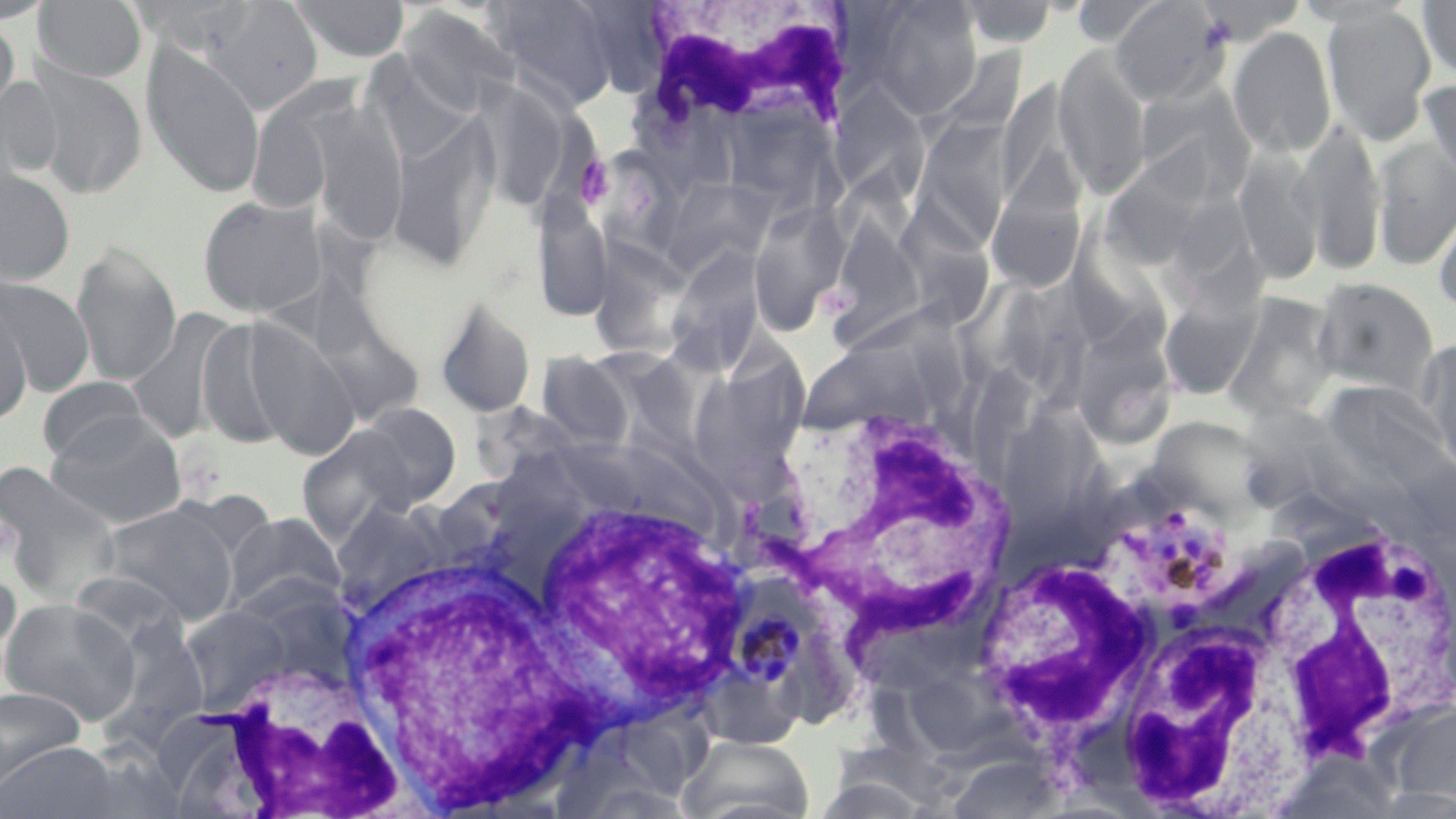

slide-level diagnosis = Plasmodium malariae
image size = 1456×819 pixels
white blood cell locations = approximate bounding boxes as [x1, y1, x2, y2] in pixels: [639, 0, 854, 131], [778, 403, 1019, 653], [516, 487, 753, 722], [1246, 504, 1451, 766], [331, 543, 604, 816], [970, 552, 1154, 744], [1108, 607, 1305, 814], [189, 661, 409, 818]
Plasmodium malariae-infected red blood cell locations = approximate bounding boxes as [x1, y1, x2, y2] in pixels: [1097, 492, 1240, 610], [727, 573, 819, 695]
preparation = thin blood film
magnification = 1000x
platelet locations = approximate bounding boxes as [x1, y1, x2, y2] in pixels: [575, 156, 615, 208]
field of view = one of a larger specimen
uninfected red blood cell locations = approximate bounding boxes as [x1, y1, x2, y2] in pixels: [33, 0, 147, 83], [128, 0, 260, 58], [206, 0, 324, 113], [289, 0, 410, 64], [484, 0, 622, 112], [861, 0, 984, 120], [1068, 0, 1169, 47], [1194, 0, 1307, 44], [1419, 0, 1456, 80], [956, 1, 1059, 48], [1110, 1, 1227, 105], [1323, 4, 1437, 146], [405, 6, 525, 116], [0, 14, 20, 122], [1229, 26, 1337, 158], [357, 34, 467, 156], [140, 41, 267, 199], [938, 47, 1026, 137], [1054, 47, 1152, 199], [26, 65, 149, 199], [0, 77, 63, 187], [1421, 78, 1456, 188], [997, 80, 1088, 211], [468, 83, 575, 210], [1134, 84, 1256, 200], [829, 87, 930, 203], [296, 98, 411, 248], [388, 114, 500, 273], [911, 117, 1017, 247], [1298, 118, 1386, 276], [1373, 137, 1456, 270], [987, 140, 1089, 290], [1098, 140, 1220, 270], [594, 147, 686, 273], [1235, 148, 1324, 285], [0, 166, 77, 286], [664, 180, 784, 285], [198, 194, 328, 319], [533, 194, 613, 323], [1433, 197, 1456, 319], [749, 199, 852, 335], [902, 203, 995, 333], [823, 207, 930, 345], [1077, 215, 1172, 347], [70, 240, 183, 388], [665, 249, 764, 378], [589, 266, 685, 367], [0, 277, 95, 397], [1311, 278, 1439, 399], [1158, 285, 1265, 401], [310, 289, 424, 434], [1223, 292, 1340, 423], [0, 294, 33, 426], [434, 295, 536, 418], [130, 308, 238, 444], [237, 314, 361, 460], [1085, 316, 1180, 447], [195, 317, 299, 449], [802, 330, 936, 436], [739, 332, 811, 462], [1420, 337, 1456, 475], [537, 352, 635, 450], [688, 375, 794, 495], [38, 376, 149, 465], [1323, 376, 1455, 518], [350, 403, 462, 510], [1004, 408, 1099, 538], [45, 412, 189, 528], [1144, 422, 1280, 511], [295, 425, 417, 543], [560, 446, 732, 536], [0, 461, 122, 607], [97, 502, 239, 625], [222, 512, 347, 616], [0, 573, 21, 674], [0, 597, 141, 725], [179, 605, 293, 711], [106, 615, 210, 745], [904, 663, 1030, 766], [0, 686, 88, 787], [1382, 701, 1456, 812], [622, 719, 728, 798], [678, 734, 815, 818], [1, 741, 122, 819], [946, 757, 1064, 817]
stain = May-Grünwald-Giemsa
modality = light microscopy